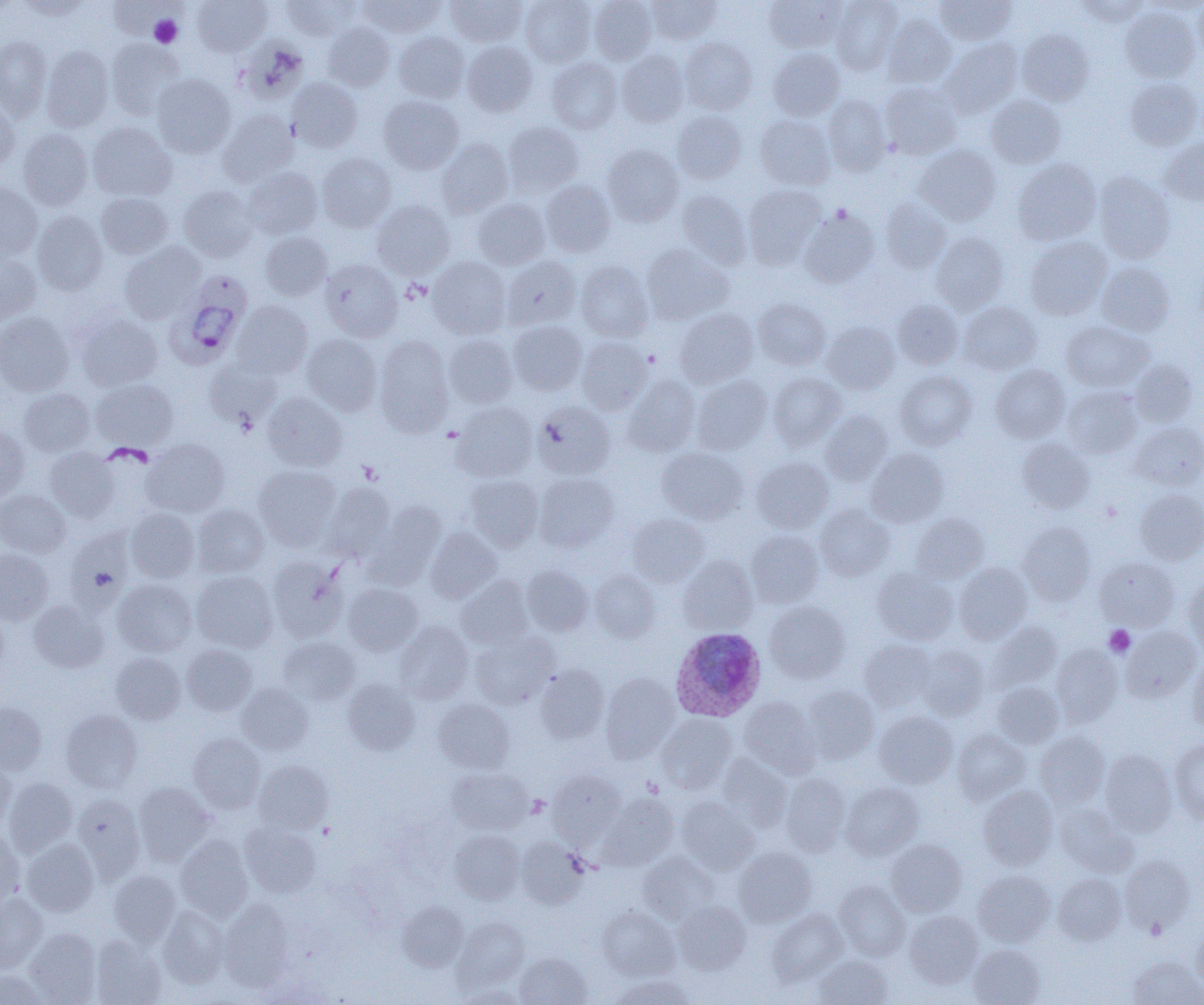
Approximate bounding boxes as (x1, y1, x2, y2) in pixels. Uninfected red blood cell locations: (15, 0, 90, 20), (193, 0, 272, 56), (281, 0, 361, 40), (358, 0, 445, 37), (445, 0, 528, 47), (520, 0, 596, 66), (589, 0, 656, 65), (645, 0, 721, 45), (764, 0, 845, 53), (831, 0, 902, 75), (935, 0, 1016, 46), (1076, 1, 1151, 25), (1194, 1, 1204, 60), (1120, 7, 1201, 82), (882, 14, 955, 88), (322, 22, 394, 91), (1017, 29, 1093, 105), (393, 31, 469, 103), (0, 36, 52, 120), (236, 37, 309, 103), (680, 37, 757, 115), (106, 38, 184, 120), (939, 38, 1022, 118), (462, 41, 537, 116), (40, 46, 114, 132), (768, 48, 844, 121), (616, 50, 690, 127), (546, 58, 622, 134), (152, 73, 237, 158), (1125, 77, 1202, 150), (287, 78, 362, 152), (880, 82, 961, 160), (379, 95, 464, 173), (822, 95, 892, 175), (986, 95, 1066, 168), (0, 101, 18, 174), (673, 110, 747, 184), (218, 111, 299, 186), (755, 114, 835, 191), (502, 121, 584, 197), (87, 122, 176, 201), (18, 128, 93, 210), (436, 138, 514, 218), (1160, 138, 1204, 205), (603, 144, 684, 227), (915, 144, 1001, 225), (316, 152, 397, 232), (1013, 159, 1101, 246), (242, 166, 322, 240), (1094, 171, 1175, 263), (540, 180, 616, 257), (0, 182, 42, 259), (179, 185, 258, 262), (743, 185, 826, 269), (676, 190, 752, 269), (96, 193, 173, 259), (473, 197, 550, 269), (881, 198, 952, 273), (372, 199, 455, 279), (800, 209, 879, 288), (32, 211, 108, 295), (260, 231, 332, 301), (931, 232, 1008, 313), (1025, 237, 1111, 319), (120, 242, 205, 323), (641, 244, 734, 325), (0, 252, 42, 324), (502, 256, 581, 330), (428, 257, 511, 339), (320, 259, 403, 341), (575, 261, 654, 341), (1097, 262, 1174, 336), (753, 298, 831, 370), (893, 299, 963, 369), (231, 301, 313, 379), (959, 301, 1041, 374), (675, 307, 758, 388), (0, 312, 74, 396), (75, 312, 162, 391), (508, 320, 587, 395), (822, 321, 900, 394), (1061, 322, 1151, 392), (302, 334, 382, 415), (444, 334, 517, 408), (374, 335, 454, 434), (576, 336, 652, 414), (205, 359, 282, 430), (1130, 359, 1198, 426), (991, 365, 1070, 443), (895, 370, 977, 450), (768, 372, 846, 449), (691, 375, 772, 454), (623, 376, 701, 455), (91, 378, 178, 451), (1062, 385, 1142, 458), (19, 388, 95, 457), (262, 393, 347, 471), (532, 401, 615, 479), (452, 402, 537, 482), (820, 411, 893, 484), (0, 422, 30, 501), (1131, 422, 1204, 490), (1017, 437, 1095, 513), (142, 438, 230, 517), (45, 447, 120, 523), (657, 447, 747, 524), (866, 448, 949, 527), (751, 457, 834, 533), (253, 465, 341, 549), (533, 473, 618, 552), (464, 474, 543, 550), (319, 483, 395, 562), (1135, 489, 1204, 564), (0, 490, 71, 557), (368, 502, 446, 584), (192, 504, 269, 577), (814, 504, 895, 581), (126, 508, 200, 582), (911, 513, 989, 583), (628, 514, 709, 586), (1018, 522, 1095, 604), (425, 528, 502, 602), (64, 529, 133, 613), (745, 530, 824, 607), (0, 549, 53, 624), (267, 556, 349, 642), (678, 556, 757, 633), (1095, 557, 1179, 630), (954, 562, 1032, 643), (522, 564, 593, 635), (872, 567, 958, 645), (191, 570, 278, 652), (589, 570, 660, 643), (457, 575, 534, 649), (1183, 576, 1204, 653), (112, 578, 197, 657), (343, 582, 423, 655), (28, 600, 108, 672), (765, 601, 850, 683), (989, 620, 1062, 691), (395, 621, 474, 704), (1121, 626, 1201, 702), (471, 632, 557, 709), (276, 636, 360, 706), (859, 639, 935, 711), (1051, 643, 1124, 726), (182, 644, 257, 716), (916, 645, 989, 719), (111, 652, 186, 724), (1187, 655, 1204, 734), (534, 664, 609, 743), (600, 673, 679, 761), (342, 678, 421, 756), (237, 682, 313, 755), (992, 682, 1063, 748), (801, 686, 879, 764), (739, 696, 820, 777), (433, 699, 514, 773), (0, 702, 47, 775), (61, 710, 143, 792), (874, 711, 958, 787), (657, 714, 736, 793), (952, 729, 1030, 804), (1034, 731, 1110, 808), (188, 733, 265, 813), (1169, 740, 1204, 825), (1099, 749, 1176, 835), (716, 753, 792, 830), (254, 760, 332, 834), (0, 761, 15, 829), (447, 768, 532, 835), (548, 770, 625, 842), (780, 773, 851, 856), (3, 778, 78, 856), (133, 782, 217, 867), (841, 782, 923, 859), (978, 785, 1058, 869), (72, 794, 145, 883), (600, 794, 679, 869), (677, 797, 759, 874), (1056, 803, 1137, 876), (241, 823, 321, 898), (0, 827, 24, 910), (450, 829, 524, 903), (176, 834, 253, 921), (21, 838, 99, 916), (515, 838, 589, 908), (886, 839, 966, 916), (734, 846, 816, 926), (637, 851, 718, 922), (1119, 854, 1196, 934), (108, 870, 181, 947), (973, 870, 1055, 946), (1054, 874, 1127, 944), (834, 880, 910, 961), (0, 892, 47, 973), (219, 899, 294, 991), (673, 900, 750, 974), (397, 902, 469, 972), (158, 905, 230, 987), (597, 907, 679, 980), (768, 909, 848, 984), (904, 910, 983, 987), (453, 916, 529, 990), (1191, 926, 1204, 991), (25, 928, 101, 1004), (91, 936, 167, 1005), (968, 945, 1045, 1005), (515, 953, 591, 1005), (814, 955, 892, 1005), (1128, 956, 1204, 1005), (0, 970, 48, 1004), (613, 975, 695, 1005), (454, 985, 525, 1005). Platelet locations: (150, 15, 182, 47), (1104, 625, 1135, 658). Plasmodium ovale-infected red blood cell locations: (166, 274, 252, 369), (669, 627, 766, 721). Slide-level diagnosis: Plasmodium ovale. 1000x magnification. One field of a larger specimen. Light microscopy. Thin blood smear. Image is 1204×1005 pixels.